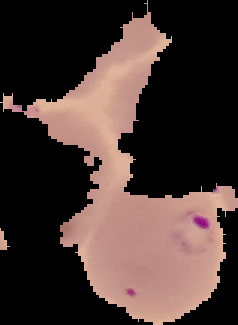

Summary:
  - Image type: segmented cell region with the area outside set to black
  - Preparation: thin blood smear
  - Result: Plasmodium parasites detected
  - Image size: 238×325 pixels